Assess this cell for malaria.
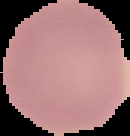

Uninfected.

Segmented cell region on a black background. Image is 130×136 pixels. From a thin blood film.